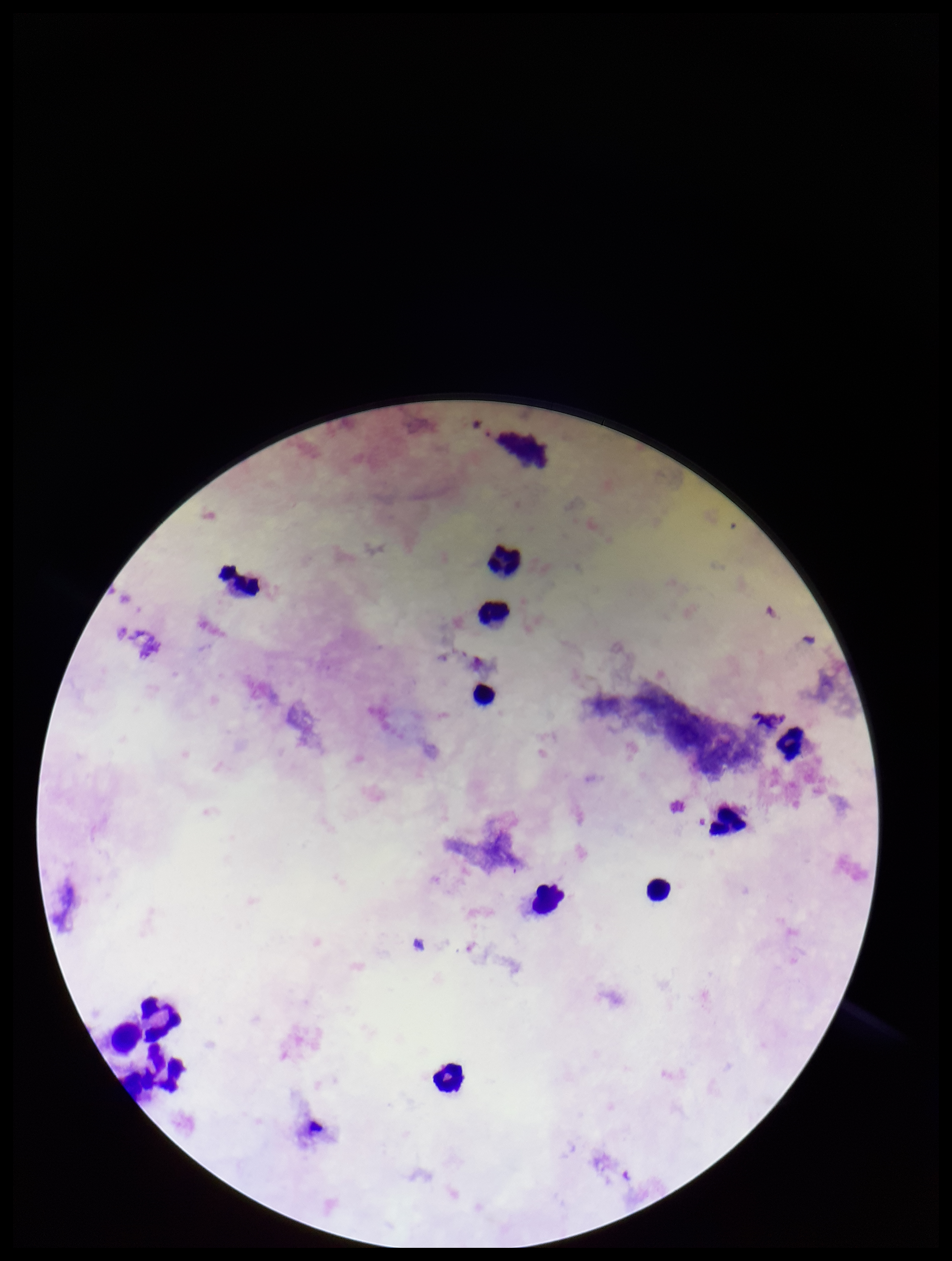

Leukocyte count: 12. Preparation: thick smear. Image is 952×1261 pixels. Patient malaria status: negative. Stained with Giemsa. Smartphone photograph taken through the eyepiece of a microscope. Parasite count: 0. Plasmodium parasites: none detected. Single field of view.